State the blood parasite species.
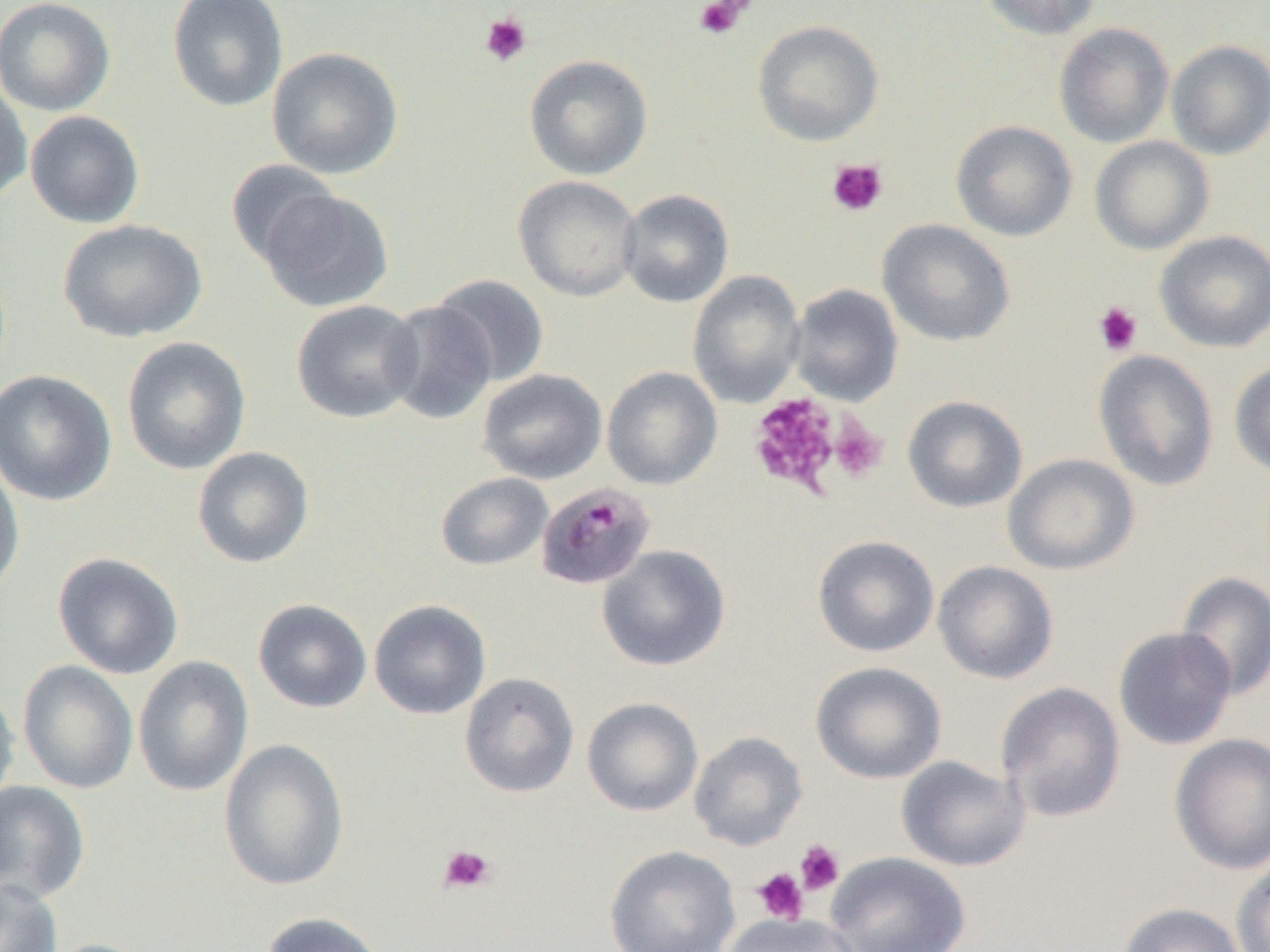

Plasmodium malariae.

Summary:
  - Coordinate format: approximate bounding boxes as named x1/y1/x2/y2 corners in pixels
  - Uninfected red blood cell locations: (x1=0, y1=0, x2=116, y2=117), (x1=167, y1=0, x2=289, y2=112), (x1=981, y1=0, x2=1103, y2=40), (x1=752, y1=19, x2=884, y2=146), (x1=1054, y1=22, x2=1174, y2=148), (x1=1166, y1=39, x2=1270, y2=160), (x1=266, y1=46, x2=404, y2=179), (x1=524, y1=54, x2=654, y2=180), (x1=0, y1=78, x2=32, y2=204), (x1=24, y1=110, x2=145, y2=229), (x1=951, y1=120, x2=1078, y2=242), (x1=1090, y1=136, x2=1214, y2=255), (x1=226, y1=159, x2=339, y2=267), (x1=513, y1=175, x2=642, y2=302), (x1=257, y1=188, x2=394, y2=313), (x1=618, y1=189, x2=735, y2=308), (x1=57, y1=219, x2=207, y2=343), (x1=877, y1=219, x2=1015, y2=347), (x1=1154, y1=230, x2=1270, y2=352), (x1=687, y1=270, x2=805, y2=408), (x1=430, y1=274, x2=550, y2=387), (x1=787, y1=284, x2=903, y2=406), (x1=291, y1=299, x2=423, y2=424), (x1=381, y1=300, x2=499, y2=425), (x1=121, y1=337, x2=251, y2=475), (x1=1093, y1=350, x2=1218, y2=492), (x1=1229, y1=359, x2=1270, y2=479), (x1=601, y1=366, x2=722, y2=491), (x1=0, y1=369, x2=117, y2=507), (x1=478, y1=369, x2=607, y2=485), (x1=902, y1=396, x2=1027, y2=512), (x1=192, y1=446, x2=315, y2=569), (x1=0, y1=451, x2=25, y2=599), (x1=1003, y1=453, x2=1139, y2=574), (x1=435, y1=472, x2=553, y2=571), (x1=813, y1=535, x2=939, y2=657), (x1=597, y1=545, x2=730, y2=670), (x1=52, y1=552, x2=184, y2=679), (x1=933, y1=560, x2=1059, y2=684), (x1=1175, y1=571, x2=1270, y2=701), (x1=252, y1=598, x2=373, y2=713), (x1=369, y1=599, x2=491, y2=720), (x1=1113, y1=626, x2=1237, y2=750), (x1=133, y1=654, x2=254, y2=797), (x1=17, y1=660, x2=139, y2=794), (x1=811, y1=661, x2=946, y2=784), (x1=460, y1=672, x2=580, y2=797), (x1=996, y1=681, x2=1126, y2=822), (x1=0, y1=688, x2=20, y2=811), (x1=582, y1=697, x2=703, y2=816), (x1=689, y1=731, x2=807, y2=850), (x1=1169, y1=733, x2=1270, y2=875), (x1=218, y1=738, x2=350, y2=891), (x1=896, y1=755, x2=1029, y2=872), (x1=0, y1=780, x2=91, y2=902), (x1=604, y1=845, x2=740, y2=952), (x1=825, y1=851, x2=970, y2=952), (x1=1232, y1=856, x2=1270, y2=952), (x1=0, y1=878, x2=63, y2=952), (x1=1118, y1=902, x2=1247, y2=952), (x1=259, y1=911, x2=390, y2=952), (x1=721, y1=913, x2=859, y2=952), (x1=39, y1=938, x2=156, y2=952)
  - Plasmodium malariae-infected red blood cell locations: (x1=536, y1=482, x2=655, y2=590)
  - Platelet locations: (x1=693, y1=0, x2=754, y2=40), (x1=479, y1=13, x2=532, y2=67), (x1=827, y1=158, x2=888, y2=217), (x1=1093, y1=302, x2=1143, y2=356), (x1=748, y1=392, x2=843, y2=499), (x1=828, y1=416, x2=888, y2=483), (x1=795, y1=840, x2=845, y2=895), (x1=438, y1=844, x2=497, y2=894), (x1=752, y1=867, x2=809, y2=925)
  - Modality: light microscopy
  - Preparation: thin blood film
  - Field of view: single
  - Image size: 1270×952 pixels
  - Magnification: 1000x